Locate and identify every blood parasite.
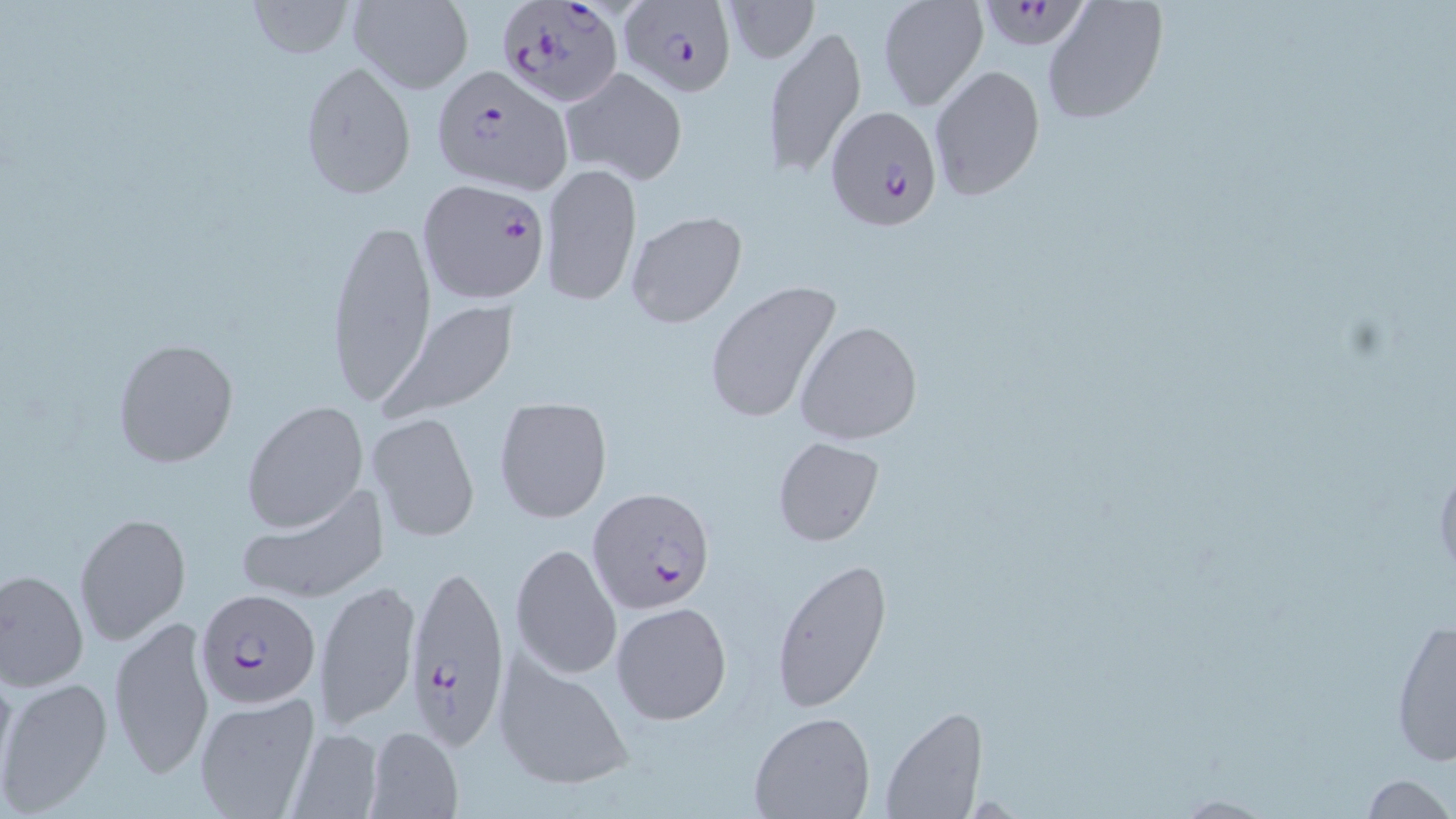
Approximate bounding boxes as (x1, y1, x2, y2) in pixels.
Plasmodium falciparum-infected red blood cells: (618, 0, 736, 95), (979, 0, 1095, 55), (498, 1, 622, 107), (431, 64, 573, 195), (823, 104, 941, 228), (417, 179, 550, 303), (588, 487, 716, 611), (403, 557, 510, 751), (194, 587, 321, 710).
No Plasmodium ovale, Plasmodium malariae, Plasmodium vivax, Babesia divergens, or Trypanosoma brucei observed.

Uninfected red blood cell locations: (245, 0, 355, 59), (347, 0, 474, 93), (724, 0, 820, 64), (876, 0, 988, 110), (1042, 1, 1168, 125), (761, 24, 866, 180), (298, 60, 418, 200), (928, 63, 1046, 201), (558, 66, 690, 187), (542, 161, 641, 307), (624, 210, 748, 328), (329, 213, 435, 406), (703, 279, 843, 426), (380, 301, 519, 419), (795, 320, 923, 446), (112, 336, 240, 470), (242, 400, 368, 533), (493, 401, 613, 524), (366, 412, 480, 542), (771, 436, 883, 544), (235, 486, 388, 606), (76, 511, 189, 645), (510, 542, 623, 681), (770, 558, 891, 717), (1, 568, 88, 690), (315, 577, 420, 731), (610, 601, 732, 725), (108, 614, 216, 779), (1388, 614, 1455, 768), (492, 648, 636, 794), (0, 678, 113, 812), (192, 690, 321, 817), (881, 707, 989, 819), (748, 709, 875, 818), (364, 725, 464, 818), (286, 727, 384, 819), (1360, 775, 1452, 817). Slide-level diagnosis: Plasmodium falciparum. Thin blood smear. Light microscopy. Image is 1456×819 pixels. Captured at 1000x magnification. May-Grünwald-Giemsa stain. One field of a larger specimen.